Assess this cell for malaria.
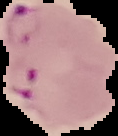
Parasitized.

preparation = thin blood film
image type = segmented cell region on a black background
image size = 118×136 pixels